Name the parasite shown.
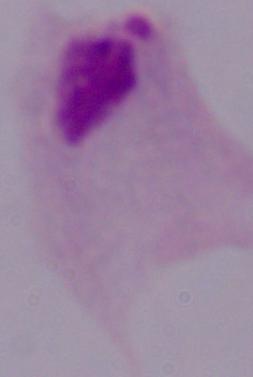

This is a trichomonad.

1000x magnification. Micrograph.